Identify the blood parasite species.
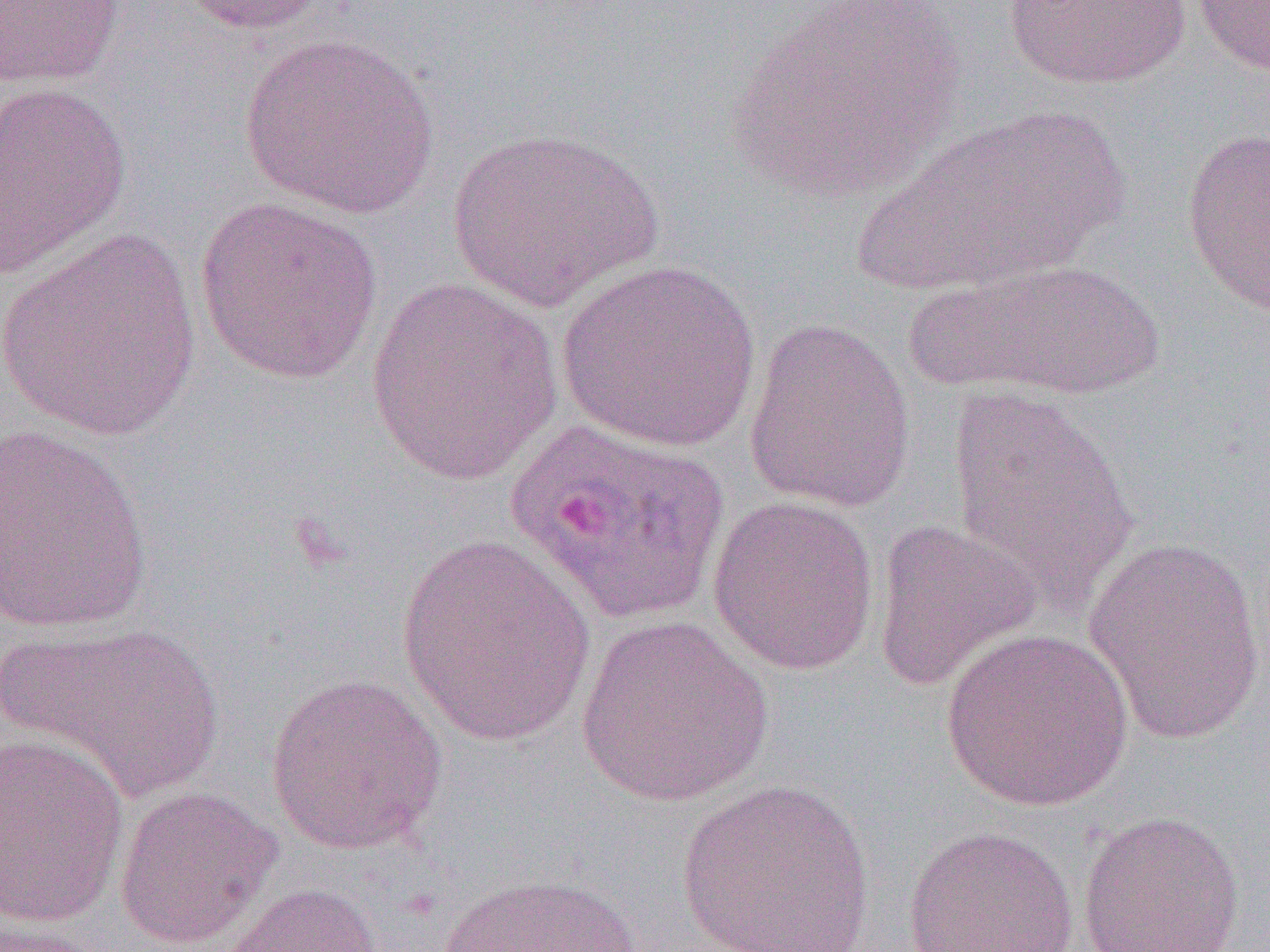
Plasmodium ovale.

Summary:
  - Coordinate format: approximate bounding boxes as (x1,y1)-(x2,y2) corner pairs in pixels
  - Uninfected red blood cell locations: (175,0)-(329,36), (1003,0)-(1191,90), (1189,0)-(1270,78), (0,1)-(126,89), (719,2)-(971,204), (239,33)-(441,220), (0,80)-(132,279), (853,106)-(1130,295), (1181,125)-(1270,316), (445,126)-(665,310), (194,197)-(385,385), (0,229)-(204,440), (557,258)-(762,452), (901,258)-(1171,401), (367,276)-(562,486), (743,318)-(916,515), (945,383)-(1141,619), (0,423)-(155,634), (707,494)-(880,676), (871,518)-(1041,691), (1082,535)-(1267,746), (395,536)-(597,748), (575,615)-(775,807), (4,621)-(226,803), (940,627)-(1134,812), (265,672)-(449,856), (0,732)-(131,928), (676,778)-(875,951), (114,784)-(282,949), (1076,810)-(1246,952), (902,825)-(1079,952), (432,873)-(650,952), (215,882)-(385,952), (0,920)-(107,951)
  - Plasmodium ovale-infected red blood cell locations: (504,419)-(730,624)
  - Magnification: 1000x
  - Modality: light microscopy
  - Field of view: single
  - Preparation: thin blood smear
  - Image size: 1270×952 pixels